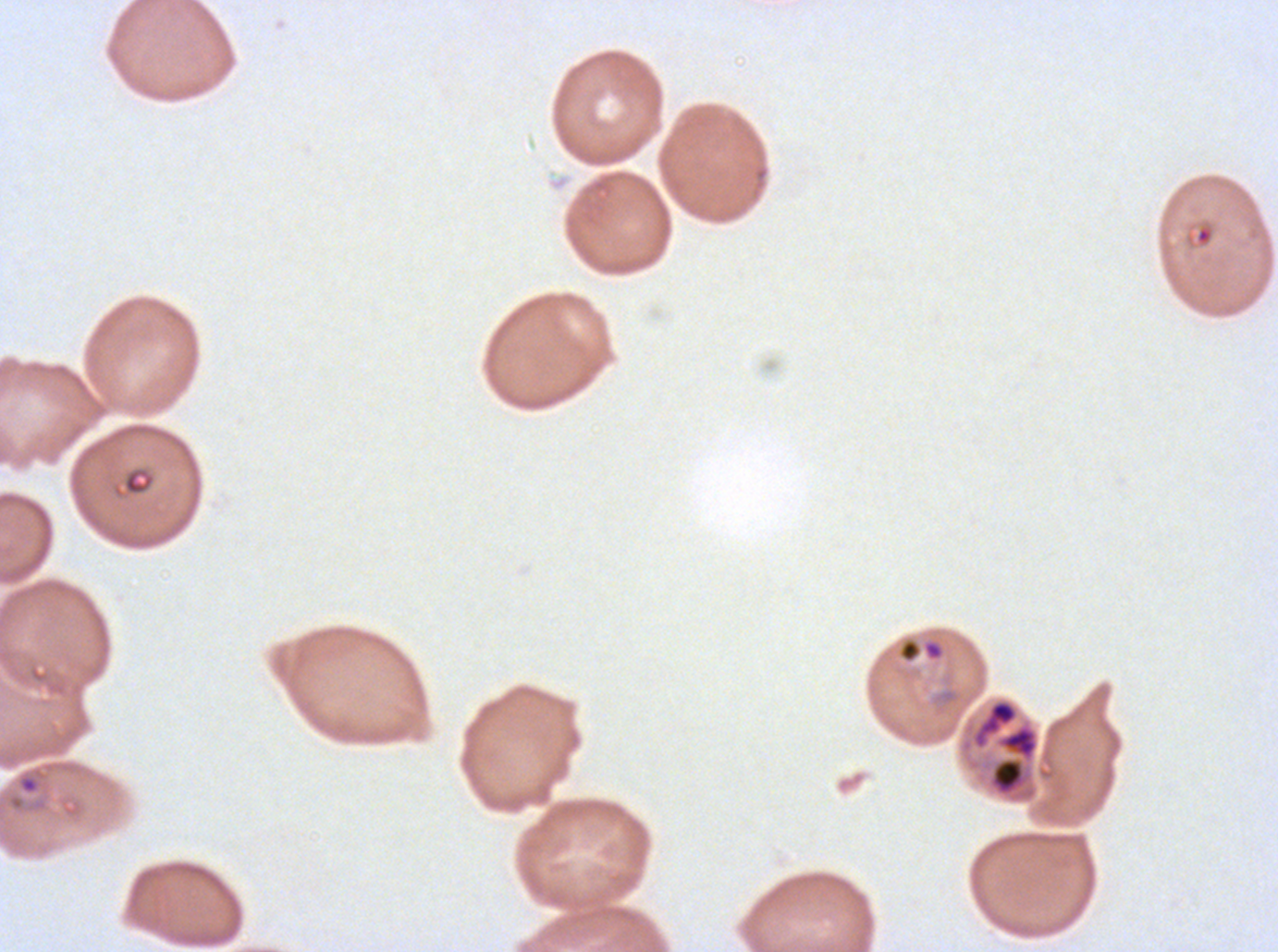

Approximate bounding rectangles given as corner coordinates in pixels from the top-left. Ring locations: (x1=896, y1=637, x2=946, y2=664), (x1=18, y1=775, x2=39, y2=794). Debris locations: (x1=1194, y1=224, x2=1214, y2=247), (x1=121, y1=466, x2=156, y2=496). Thin blood smear. Image is 1278×952 pixels. Ex-vivo P. falciparum culture from a patient in The Gambia, grown for 24 to 48 hours. One sub-image of a larger composite. Giemsa stain.